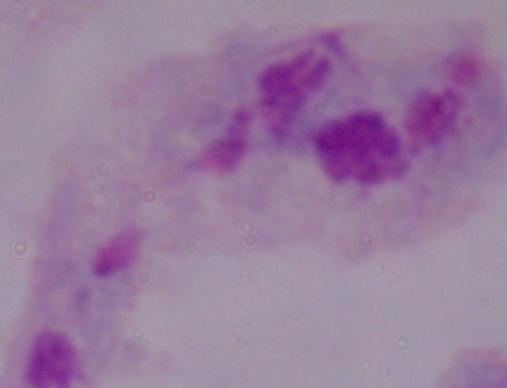
identification = trichomonad
magnification = 1000x
modality = micrograph